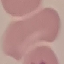
Malaria status: uninfected. Thin blood smear. Photographed with a smartphone camera at the microscope eyepiece. Giemsa-stained preparation. Automatically extracted cell patch, resized to 64 × 64 pixels.